Assess this cell for malaria.
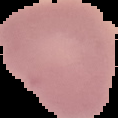

Uninfected.

{
  "preparation": "thin blood smear",
  "image_type": "segmented cell region with the area outside set to black",
  "image_size": "118×118 pixels"
}